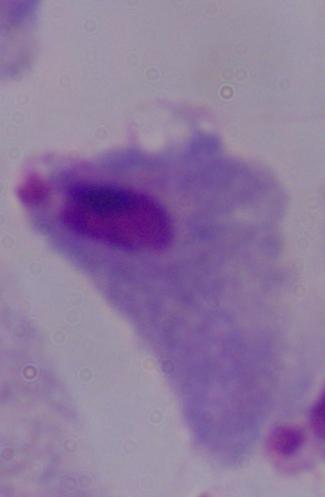

{
  "modality": "photomicrograph",
  "magnification": "1000x",
  "identification": "trichomonad"
}